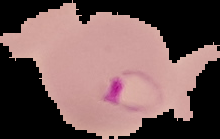

Image is 220×139 pixels. Malaria status: parasitized. From a thin blood film. Cell region segmented out of the field of view; the surrounding area is masked to black.